Classify this cell by malaria status.
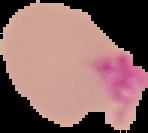

Uninfected.

Summary:
  - Preparation: thin blood film
  - Image type: segmented cell region on a black background
  - Image size: 148×133 pixels